Classify this cell by malaria status.
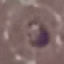
It is parasitized.

stain = Giemsa
image type = automatically extracted cell patch, resized to 64 × 64 pixels
preparation = thin smear
capture = smartphone through the microscope eyepiece